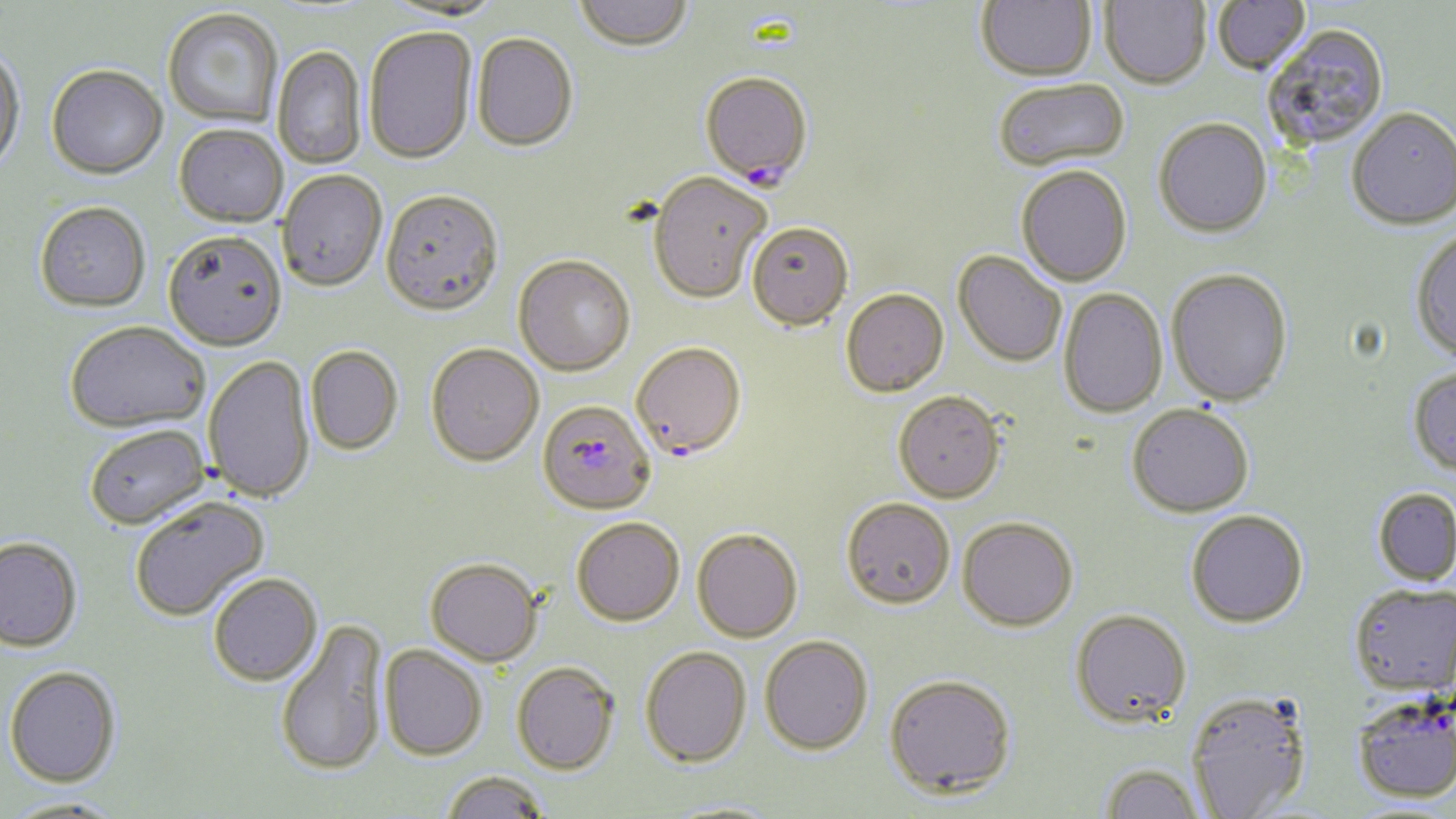 Approximate bounding boxes as (x1,y1)-(x2,y2) corner pairs in pixels. Uninfected red blood cell locations: (574,0)-(693,54), (976,0)-(1097,83), (1212,0)-(1310,75), (379,1)-(506,23), (1099,1)-(1211,91), (162,9)-(283,130), (1262,25)-(1390,151), (363,27)-(477,166), (471,33)-(578,153), (273,46)-(367,170), (0,48)-(26,178), (46,67)-(168,183), (994,80)-(1130,175), (1347,107)-(1456,230), (1154,118)-(1272,238), (174,126)-(287,229), (1017,167)-(1133,288), (277,171)-(387,293), (648,172)-(771,303), (380,192)-(504,319), (35,204)-(151,314), (747,221)-(854,331), (1409,229)-(1456,361), (162,233)-(286,353), (953,251)-(1066,367), (513,255)-(636,377), (1166,268)-(1293,406), (1058,288)-(1168,418), (841,289)-(949,397), (65,323)-(210,435), (630,342)-(746,459), (425,343)-(544,467), (305,346)-(404,455), (203,355)-(316,504), (1407,366)-(1456,475), (893,390)-(1007,503), (1127,403)-(1254,516), (85,426)-(210,531), (1372,487)-(1456,586), (130,497)-(271,623), (841,497)-(955,609), (1186,509)-(1308,626), (957,516)-(1078,631), (571,517)-(684,626), (692,528)-(803,642), (0,539)-(83,655), (425,558)-(543,667), (208,574)-(323,688), (1349,582)-(1456,695), (1070,608)-(1192,727), (275,620)-(389,778), (759,636)-(873,754), (379,645)-(486,761), (640,646)-(752,767), (512,662)-(621,776), (4,668)-(121,789), (883,672)-(1017,798), (1186,690)-(1312,818), (1351,692)-(1455,803), (1099,763)-(1206,819), (440,771)-(551,819), (2,798)-(127,817), (658,799)-(786,818). Plasmodium falciparum-infected red blood cell locations: (700,72)-(813,188), (536,399)-(656,516). Slide-level diagnosis: Plasmodium falciparum. Thin blood film. Light microscopy. Image is 1456×819 pixels. May-Grünwald-Giemsa-stained preparation. One field of a larger specimen. Captured at 1000x magnification.